State which cell type is depicted.
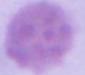

An erythrocyte.

Summary:
  - Magnification: 1000x
  - Modality: photomicrograph